Locate and identify every blood parasite.
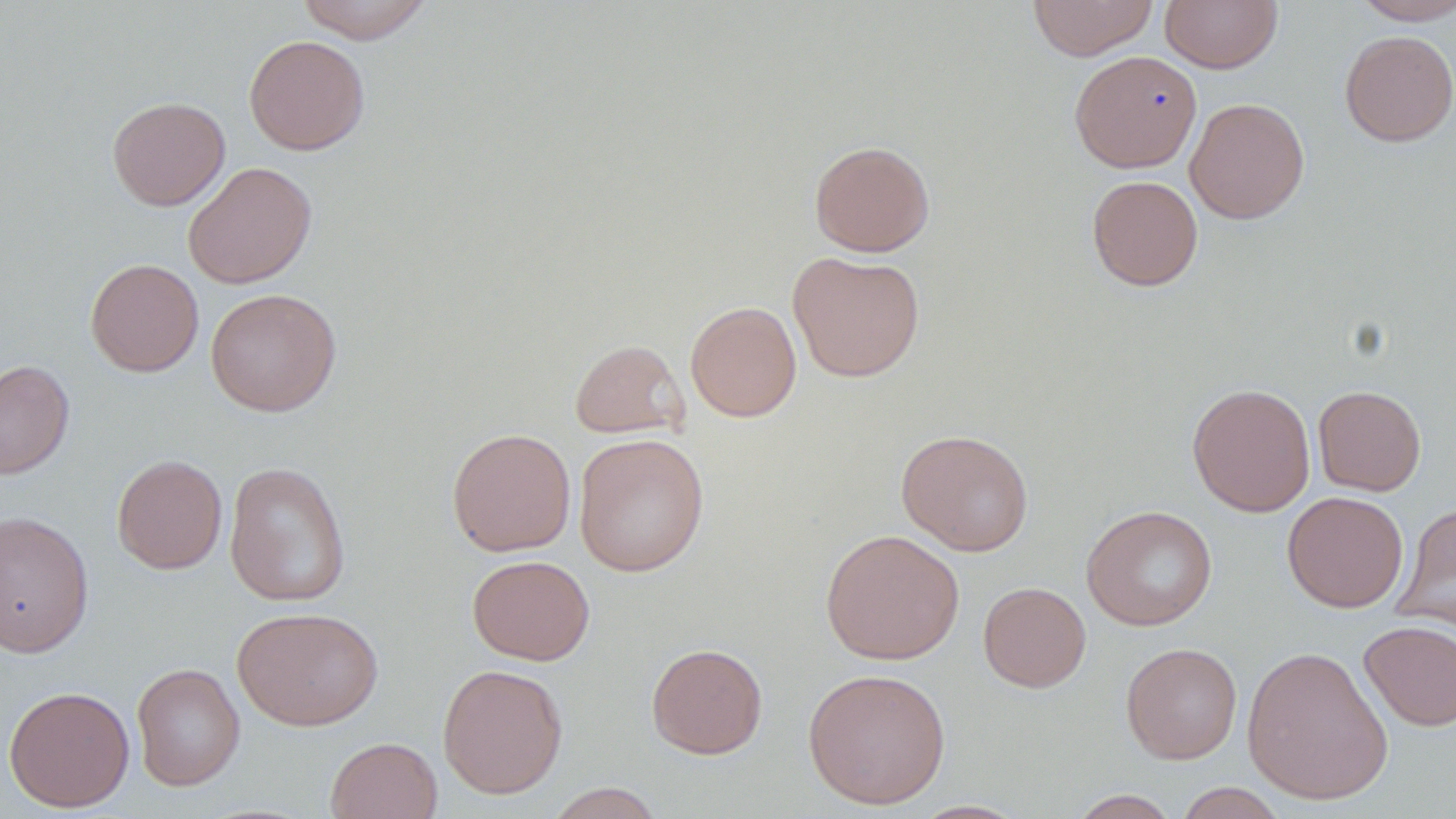

No blood parasites observed.

Approximate bounding boxes as [x1, y1, x2, y2] in pixels. Uninfected red blood cell locations: [296, 0, 435, 44], [1028, 0, 1158, 60], [1159, 0, 1283, 73], [1350, 0, 1456, 25], [1339, 30, 1456, 147], [243, 34, 370, 155], [1068, 49, 1202, 173], [107, 96, 230, 211], [1184, 97, 1310, 224], [809, 139, 935, 257], [183, 161, 317, 289], [1086, 175, 1203, 291], [787, 251, 926, 383], [85, 259, 204, 377], [205, 287, 342, 417], [685, 301, 801, 422], [569, 338, 689, 439], [0, 359, 75, 480], [1187, 383, 1316, 516], [1313, 384, 1426, 496], [446, 427, 577, 557], [895, 429, 1035, 556], [573, 432, 710, 576], [111, 453, 228, 574], [224, 460, 351, 606], [1282, 491, 1409, 613], [1393, 502, 1456, 632], [1081, 504, 1218, 631], [0, 510, 94, 658], [820, 528, 964, 665], [467, 554, 595, 664], [977, 581, 1091, 693], [232, 606, 384, 731], [1359, 620, 1456, 731], [646, 642, 768, 759], [1121, 642, 1242, 763], [1241, 644, 1394, 805], [131, 662, 245, 792], [437, 663, 568, 799], [803, 666, 951, 810], [3, 685, 136, 812], [325, 736, 443, 819], [543, 782, 666, 818], [1173, 782, 1289, 818], [1067, 789, 1182, 818], [908, 800, 1031, 818]. Slide-level diagnosis: no evidence of blood parasites. Captured at 1000x magnification. Thin blood film. One field of a larger specimen. Light microscopy. May-Grünwald-Giemsa stain. Image is 1456×819 pixels.